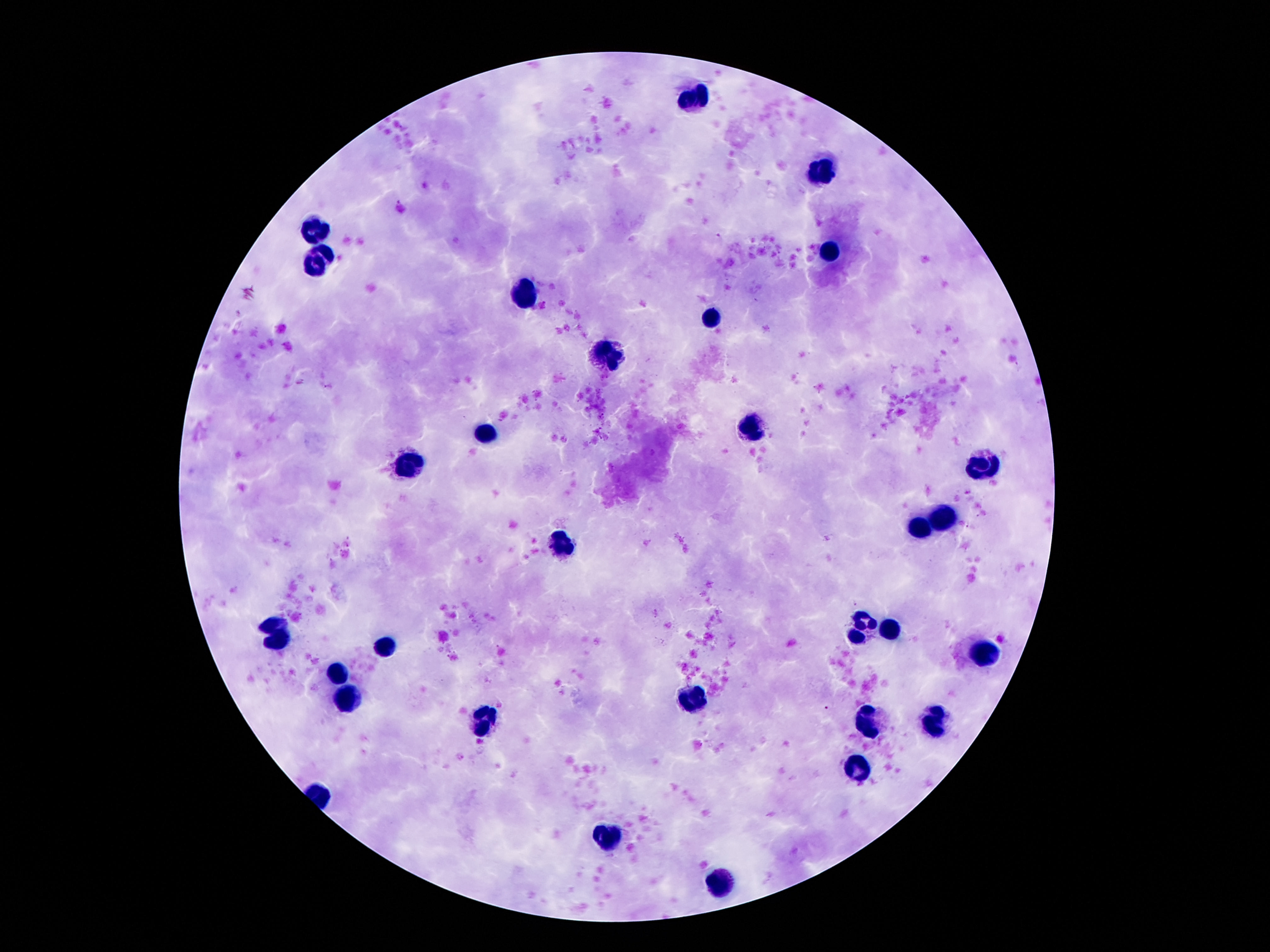

Approximate centers as (x, y) in pixels.
Summary:
  - Leukocyte locations: (694, 91), (823, 169), (315, 230), (829, 248), (315, 263), (528, 291), (709, 319), (608, 352), (750, 426), (489, 431), (985, 465), (409, 468), (941, 515), (918, 528), (564, 545), (864, 617), (271, 621), (890, 632), (853, 638), (280, 645), (383, 645), (982, 650), (338, 673), (345, 701), (692, 701), (483, 721), (868, 723), (935, 725), (855, 769), (608, 838), (720, 879)
  - Field of view: one from this slide
  - Image size: 1270×952 pixels
  - Patient malaria status: negative
  - Magnification: 100x
  - Capture: smartphone camera through the microscope eyepiece
  - Stain: Giemsa
  - Preparation: thick blood smear